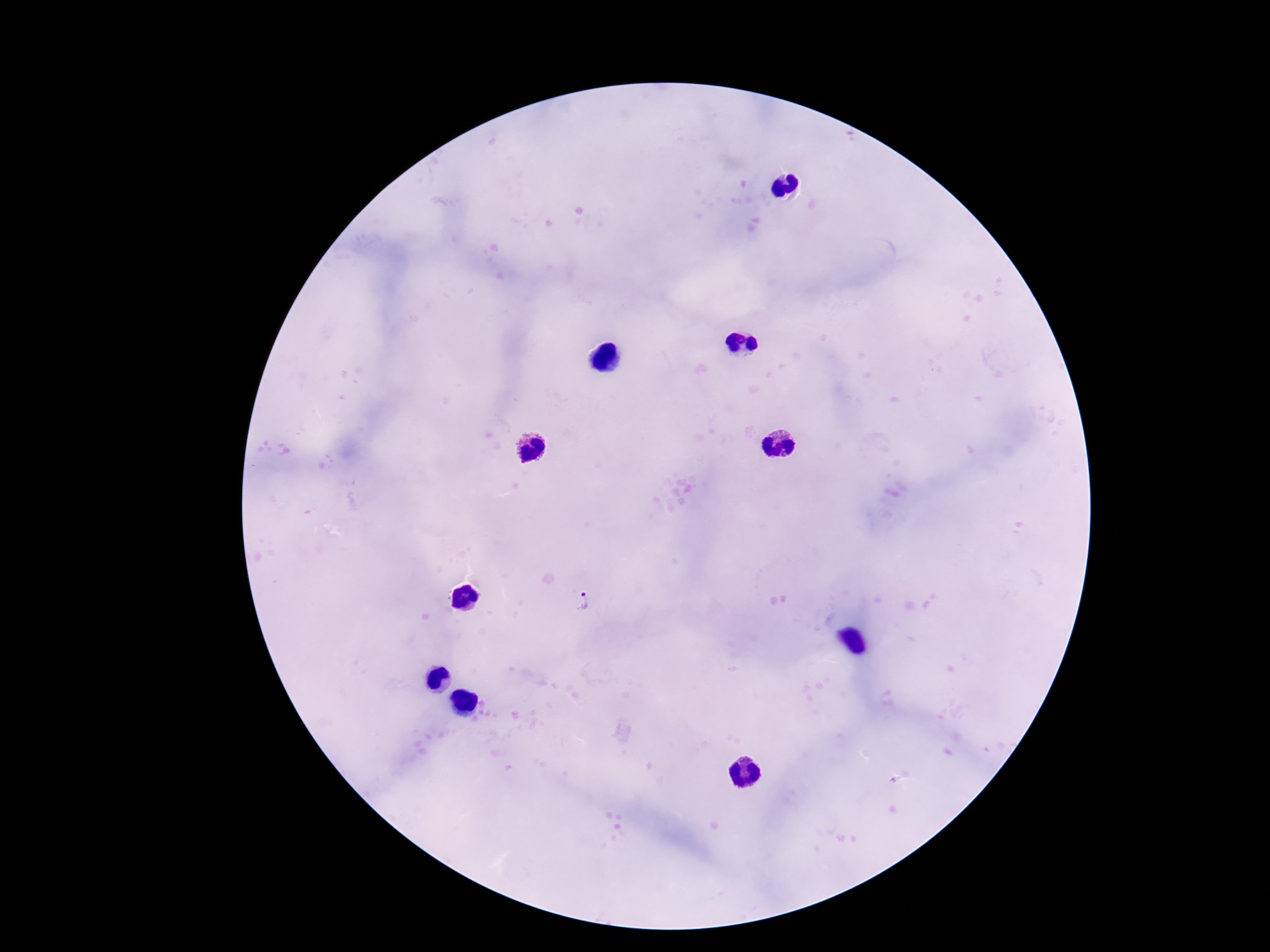

Approximate centers as [x, y] in pixels.
Summary:
  - Plasmodium parasite locations: [579, 605]
  - Field of view: one from this slide
  - Capture: smartphone camera through the microscope eyepiece
  - Stain: Giemsa
  - Magnification: 100x
  - Image size: 1270×952 pixels
  - Patient malaria status: infected
  - Preparation: thick blood smear